Assess the morphology of the erythrocytes.
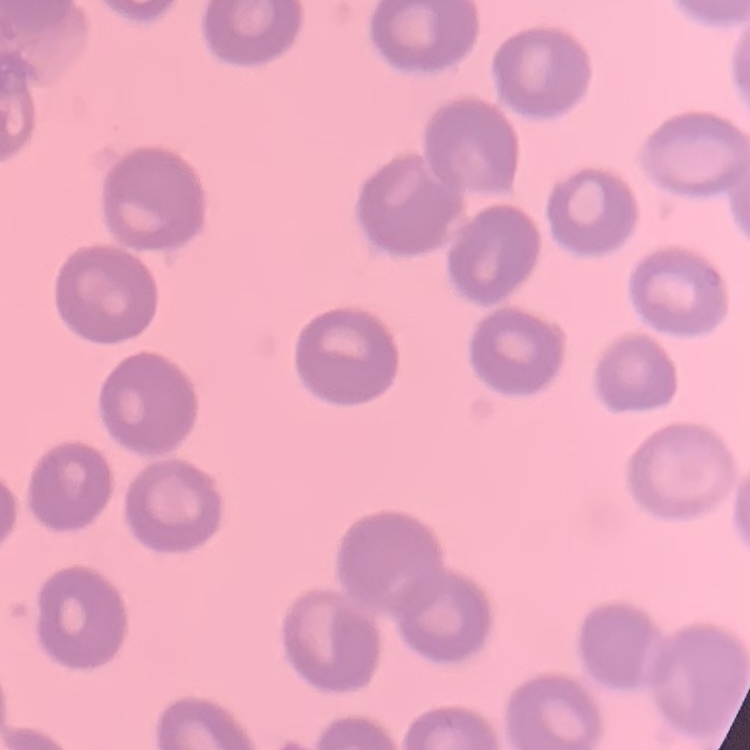

No rouleaux formation.

Field's or Giemsa stain. One tile cut from a larger photomicrograph. Thin blood smear.